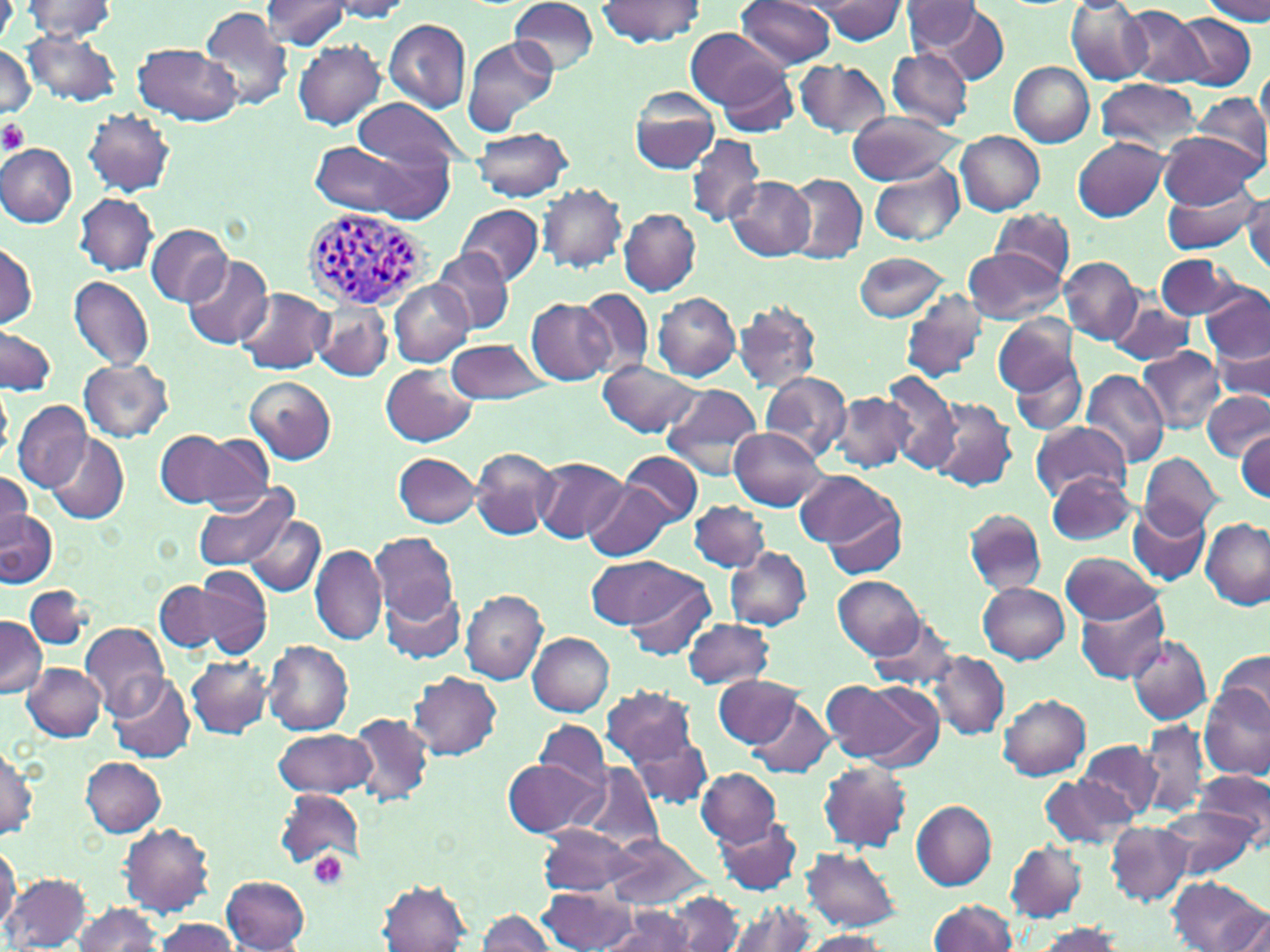
Summary:
  - Coordinate format: approximate bounding boxes as (x1,y1)-(x2,y2) corner pairs in pixels
  - Platelet locations: (0,119)-(29,157), (309,852)-(348,889)
  - Uninfected red blood cell locations: (508,0)-(598,74), (597,0)-(705,49), (737,0)-(837,69), (1202,0)-(1269,24), (20,1)-(121,41), (261,1)-(353,50), (325,1)-(417,21), (811,1)-(909,45), (901,2)-(985,54), (1066,2)-(1149,85), (270,3)-(368,90), (1121,5)-(1208,85), (199,6)-(294,111), (921,6)-(1009,83), (1175,15)-(1256,89), (383,18)-(470,113), (685,28)-(787,110), (22,30)-(123,107), (462,34)-(558,136), (292,40)-(385,131), (1,43)-(37,122), (134,43)-(241,127), (884,48)-(973,128), (794,60)-(892,139), (1009,61)-(1095,146), (716,64)-(799,138), (1257,64)-(1270,145), (1095,78)-(1201,156), (628,86)-(722,175), (1192,91)-(1269,173), (354,97)-(467,172), (82,109)-(177,198), (846,110)-(961,184), (471,127)-(573,201), (1157,130)-(1262,210), (955,131)-(1045,215), (685,133)-(767,228), (1073,137)-(1168,221), (1,142)-(78,227), (308,142)-(431,218), (868,161)-(965,247), (783,173)-(867,263), (725,175)-(816,260), (1159,182)-(1263,253), (536,183)-(628,273), (1244,192)-(1270,274), (75,193)-(157,275), (455,204)-(544,287), (618,207)-(701,295), (991,208)-(1074,284), (144,223)-(234,307), (1,243)-(37,330), (962,248)-(1066,324), (431,249)-(513,334), (853,251)-(951,322), (181,254)-(274,349), (1157,254)-(1242,321), (402,256)-(502,388), (1060,257)-(1142,342), (1175,263)-(1263,350), (68,277)-(153,372), (389,281)-(474,367), (235,286)-(334,374), (1202,286)-(1270,365), (577,287)-(656,378), (898,291)-(988,384), (653,293)-(740,382), (525,298)-(617,385), (1108,299)-(1199,366), (733,301)-(823,393), (316,303)-(393,384), (994,314)-(1079,397), (1,327)-(57,396), (445,339)-(550,403), (1211,340)-(1269,406), (1138,346)-(1226,433), (1008,358)-(1087,435), (79,359)-(174,442), (599,361)-(703,437), (381,364)-(478,447), (1081,368)-(1168,469), (879,369)-(962,472), (759,370)-(852,460), (245,376)-(336,464), (0,383)-(13,464), (660,383)-(764,476), (1204,390)-(1269,461), (831,392)-(915,473), (927,398)-(1017,492), (13,401)-(90,493), (1031,419)-(1130,501), (730,426)-(829,510), (154,429)-(258,507), (1235,429)-(1268,501), (47,433)-(130,524), (471,446)-(559,541), (617,451)-(701,527), (393,452)-(482,527), (1138,452)-(1222,534), (533,456)-(627,544), (797,471)-(904,560), (0,472)-(35,548), (1046,472)-(1138,546), (189,481)-(301,572), (585,481)-(673,561), (689,500)-(768,572), (824,501)-(909,577), (1128,503)-(1210,585), (0,509)-(57,587), (963,510)-(1045,595), (245,514)-(325,596), (1201,519)-(1268,608), (369,533)-(459,623), (309,545)-(387,645), (724,546)-(811,629), (1060,550)-(1161,624), (584,556)-(701,628), (178,566)-(272,659), (833,575)-(923,659), (624,576)-(717,662), (380,581)-(467,664), (154,582)-(232,651), (977,582)-(1069,664), (25,586)-(92,651), (460,587)-(549,684), (1075,592)-(1169,684), (866,612)-(958,692), (0,616)-(46,698), (682,618)-(774,689), (698,621)-(786,743), (81,622)-(170,715), (527,631)-(614,715), (1126,633)-(1212,725), (262,640)-(354,736), (1215,649)-(1270,727), (931,651)-(1009,739), (185,653)-(274,740), (22,663)-(106,741), (408,671)-(502,761), (107,674)-(194,764), (714,674)-(800,747), (822,677)-(937,765), (1201,684)-(1269,779), (601,685)-(698,769), (999,693)-(1092,780), (749,696)-(835,778), (349,713)-(434,806), (535,718)-(610,792), (1135,719)-(1210,819), (628,728)-(714,809), (271,729)-(377,799), (1077,741)-(1162,821), (1,745)-(39,841), (81,757)-(166,837), (503,758)-(602,838), (817,760)-(912,853), (574,762)-(664,855), (697,768)-(782,847), (1194,770)-(1268,850), (1041,773)-(1137,851), (277,788)-(363,867), (911,799)-(997,889), (1161,807)-(1256,882), (716,817)-(800,894), (1105,820)-(1193,906), (119,823)-(215,915), (536,825)-(642,896), (604,835)-(709,909), (1006,841)-(1086,922), (0,842)-(21,932), (802,847)-(901,931), (3,872)-(92,951), (221,876)-(311,951), (1169,876)-(1266,952), (377,881)-(473,951), (538,888)-(640,952), (667,891)-(746,952), (929,899)-(1018,952), (725,900)-(819,952), (70,901)-(163,952), (600,904)-(698,952), (1228,909)-(1270,952), (476,910)-(558,952), (150,917)-(243,952), (1029,922)-(1125,951), (797,931)-(892,952)
  - Plasmodium vivax-infected red blood cell locations: (304,209)-(432,312)
  - Slide-level diagnosis: Plasmodium vivax
  - Magnification: 1000x
  - Field of view: single
  - Preparation: thin blood film
  - Image size: 1270×952 pixels
  - Modality: light microscopy
  - Stain: May-Grünwald-Giemsa